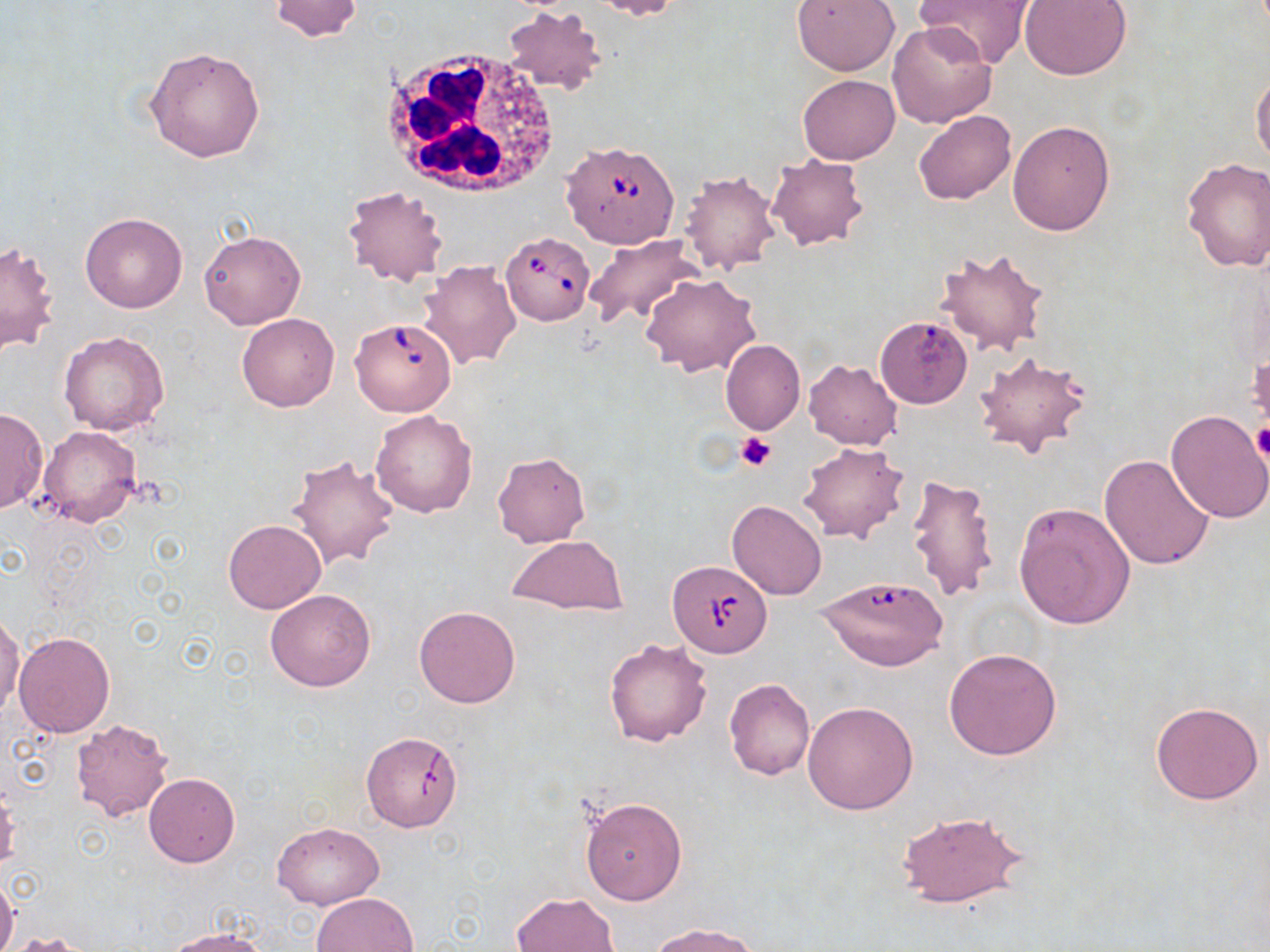

Summary:
  - Coordinate format: approximate bounding boxes as [x1, y1, x2, y2] in pixels
  - Uninfected red blood cell locations: [269, 0, 364, 42], [588, 0, 683, 19], [792, 0, 900, 76], [916, 0, 1036, 69], [1020, 0, 1132, 81], [502, 6, 605, 93], [887, 21, 997, 129], [145, 45, 266, 163], [1251, 71, 1270, 169], [798, 74, 899, 163], [913, 110, 1016, 204], [1006, 120, 1114, 237], [768, 154, 868, 251], [1181, 158, 1270, 275], [679, 170, 781, 275], [342, 184, 448, 288], [80, 212, 188, 313], [199, 231, 304, 329], [583, 235, 701, 328], [0, 240, 60, 355], [934, 246, 1050, 355], [417, 258, 522, 370], [640, 272, 762, 377], [236, 312, 340, 412], [875, 321, 968, 410], [59, 331, 170, 435], [721, 339, 805, 434], [974, 350, 1095, 460], [803, 359, 901, 449], [0, 408, 47, 513], [1166, 409, 1270, 525], [370, 410, 478, 517], [38, 425, 142, 528], [798, 441, 909, 544], [491, 452, 590, 547], [1100, 454, 1214, 570], [285, 455, 401, 571], [904, 475, 1000, 604], [726, 499, 827, 600], [1013, 501, 1135, 629], [223, 519, 326, 614], [507, 534, 629, 616], [265, 587, 376, 692], [413, 605, 520, 709], [1, 612, 23, 716], [13, 632, 115, 737], [604, 637, 713, 747], [944, 648, 1063, 760], [723, 678, 815, 782], [802, 700, 918, 815], [1150, 701, 1265, 805], [69, 716, 175, 823], [362, 731, 463, 832], [143, 774, 240, 867], [580, 798, 688, 904], [896, 810, 1028, 910], [273, 822, 381, 910], [0, 878, 19, 952], [312, 892, 419, 952], [510, 892, 620, 952], [650, 921, 759, 951], [162, 929, 271, 952]
  - Babesia divergens-infected red blood cell locations: [564, 139, 679, 246], [500, 232, 594, 325], [350, 316, 457, 416], [666, 561, 771, 658], [816, 575, 950, 673]
  - Platelet locations: [1251, 423, 1270, 462], [736, 433, 777, 471]
  - White blood cell locations: [382, 50, 562, 201]
  - Slide-level diagnosis: Babesia divergens
  - Stain: May-Grünwald-Giemsa
  - Field of view: single
  - Modality: optical microscopy
  - Image size: 1270×952 pixels
  - Magnification: 1000x
  - Preparation: thin blood smear